Name the cell type shown.
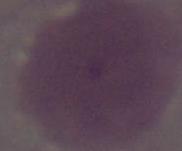

This is an erythrocyte.

Summary:
  - Magnification: 1000x
  - Modality: photomicrograph